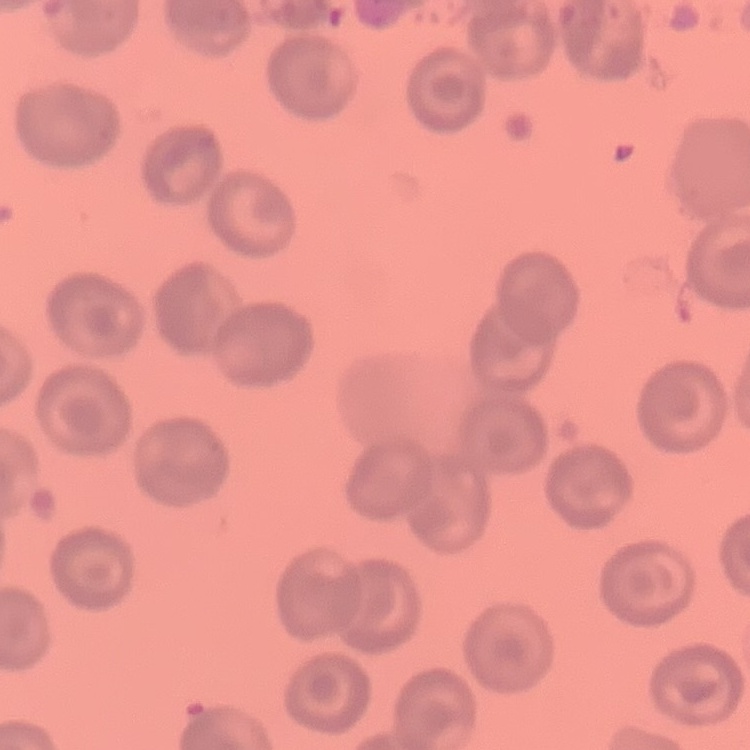
Summary:
  - Red blood cell morphology: no rouleaux formation
  - Image type: square crop of a larger photomicrograph
  - Stain: Field's or Giemsa
  - Preparation: thin blood smear